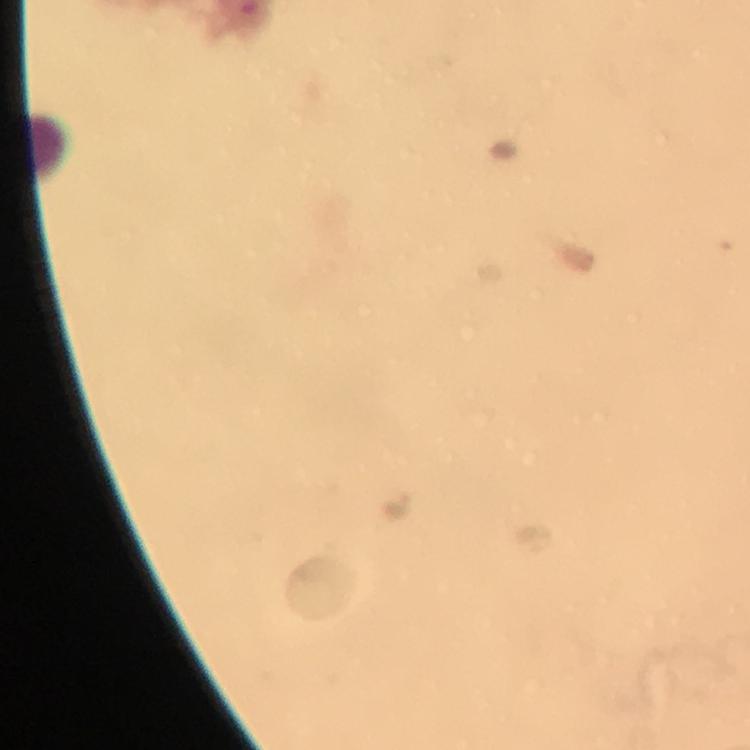

context = from a malaria diagnostic workup
cropped from = one field of view
magnification = 100x
image size = 750×750 pixels
stain = Giemsa
capture = smartphone photograph through a microscope
immersion oil = applied
preparation = thick blood film
leukocyte locations = approximate object centers, in pixels from the top-left corner: (x=49, y=143)
malaria parasites = none seen